Locate every blood parasite and identify its species.
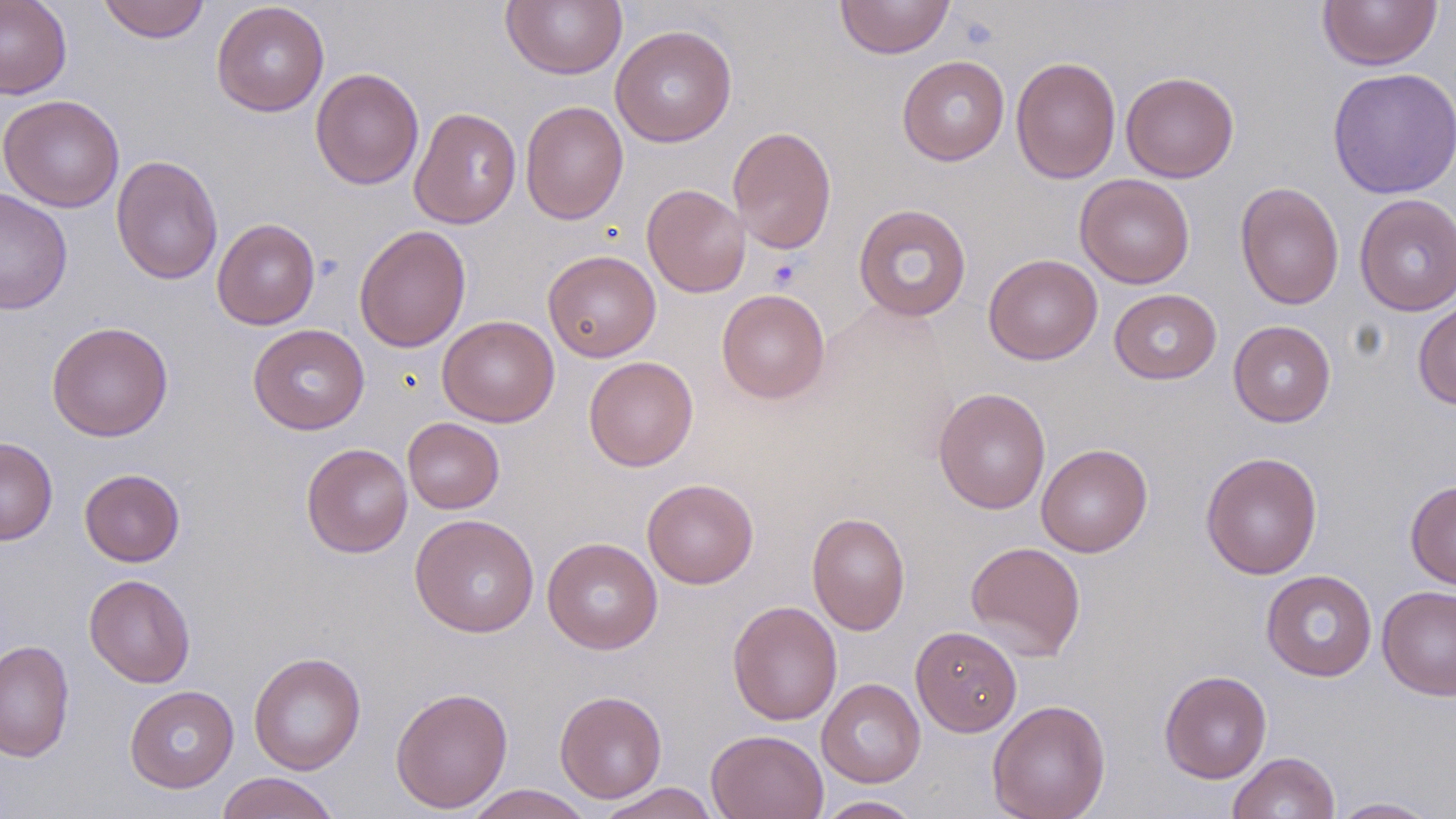

No blood parasites seen.

slide-level diagnosis = negative for blood parasites
stain = May-Grünwald-Giemsa
uninfected red blood cell locations = approximate bounding boxes as (x1, y1, x2, y2) in pixels: (0, 0, 72, 99), (97, 0, 210, 43), (501, 0, 627, 80), (835, 0, 955, 58), (1317, 0, 1442, 71), (211, 1, 330, 117), (610, 24, 737, 147), (897, 55, 1010, 165), (1010, 56, 1121, 184), (1327, 67, 1456, 199), (310, 68, 424, 189), (1121, 71, 1239, 183), (0, 95, 125, 212), (520, 101, 628, 225), (409, 106, 521, 229), (727, 126, 837, 254), (111, 155, 223, 285), (1075, 174, 1195, 289), (1235, 181, 1345, 311), (642, 184, 751, 298), (0, 187, 73, 315), (1354, 193, 1456, 316), (853, 204, 971, 322), (212, 218, 320, 330), (354, 224, 471, 353), (542, 249, 661, 362), (983, 253, 1102, 365), (716, 288, 830, 404), (1109, 289, 1221, 384), (1413, 297, 1456, 410), (437, 315, 559, 427), (1228, 320, 1336, 427), (46, 321, 174, 441), (248, 324, 370, 435), (584, 356, 698, 472), (933, 387, 1051, 515), (403, 417, 504, 514), (0, 436, 58, 545), (301, 443, 413, 558), (1036, 444, 1153, 557), (1201, 451, 1323, 579), (79, 468, 185, 567), (642, 478, 759, 589), (1405, 480, 1456, 590), (806, 512, 911, 635), (410, 513, 539, 637), (542, 537, 663, 654), (965, 541, 1086, 661), (1261, 569, 1377, 682), (84, 574, 195, 688), (1376, 585, 1456, 700), (728, 600, 843, 726), (910, 626, 1022, 736), (0, 640, 75, 762), (248, 651, 366, 774), (1159, 669, 1272, 783), (817, 678, 925, 788), (124, 685, 239, 793), (390, 686, 513, 814), (554, 690, 667, 803), (987, 699, 1111, 819), (707, 729, 828, 819), (1227, 751, 1340, 818), (216, 771, 341, 819), (594, 783, 720, 818), (463, 785, 595, 818), (814, 796, 924, 818), (1328, 797, 1443, 818)
field of view = one of a larger specimen
magnification = 1000x
modality = optical microscopy
preparation = thin blood smear
image size = 1456×819 pixels
platelet locations = approximate bounding boxes as (x1, y1, x2, y2) in pixels: (767, 259, 801, 290)